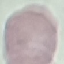

Summary:
  - Result: negative for malaria parasites
  - Image type: automatically extracted cell patch, resized to 64 × 64 pixels
  - Capture: smartphone camera at the microscope eyepiece
  - Stain: Giemsa
  - Preparation: thin smear